Assess this cell for malaria.
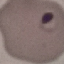

It is parasitized.

Thin smear of blood. Giemsa-stained preparation. Acquired by smartphone through the microscope eyepiece. Automatically extracted cell patch, resized to 64 × 64 pixels.